Describe the morphology of the red blood cells.
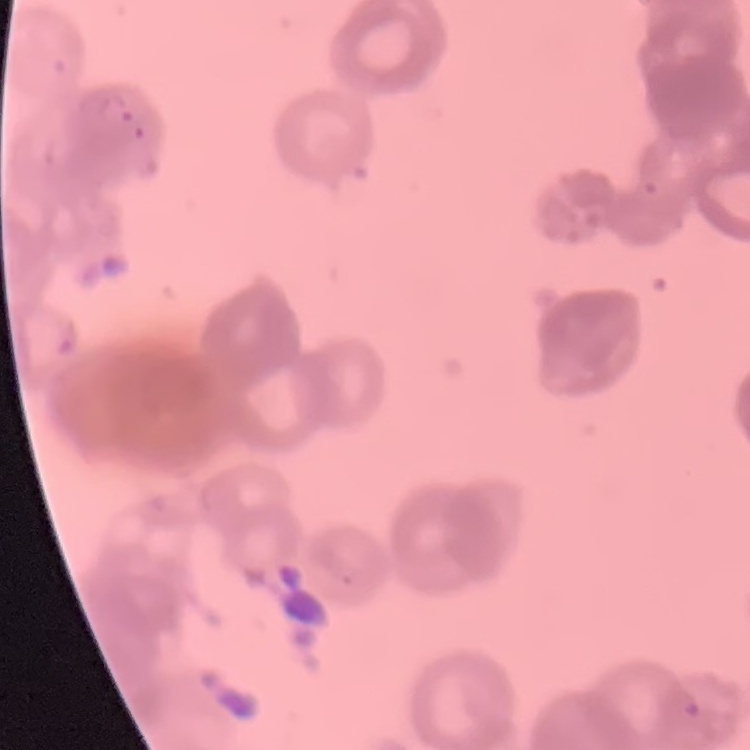
They show rouleaux formation.

Summary:
  - Stain: Field's or Giemsa
  - Image type: square crop of a larger photomicrograph
  - Preparation: thin peripheral smear